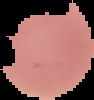

Summary:
  - Image type: segmented cell region with the area outside set to black
  - Preparation: thin blood film
  - Malaria status: uninfected
  - Image size: 94×100 pixels